Classify this cell by malaria status.
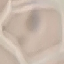

It is uninfected.

stain = Giemsa
preparation = thin blood film
capture = smartphone camera at the microscope eyepiece
image type = automatically extracted cell patch, resized to 64 × 64 pixels